Locate every uninfected red blood cell.
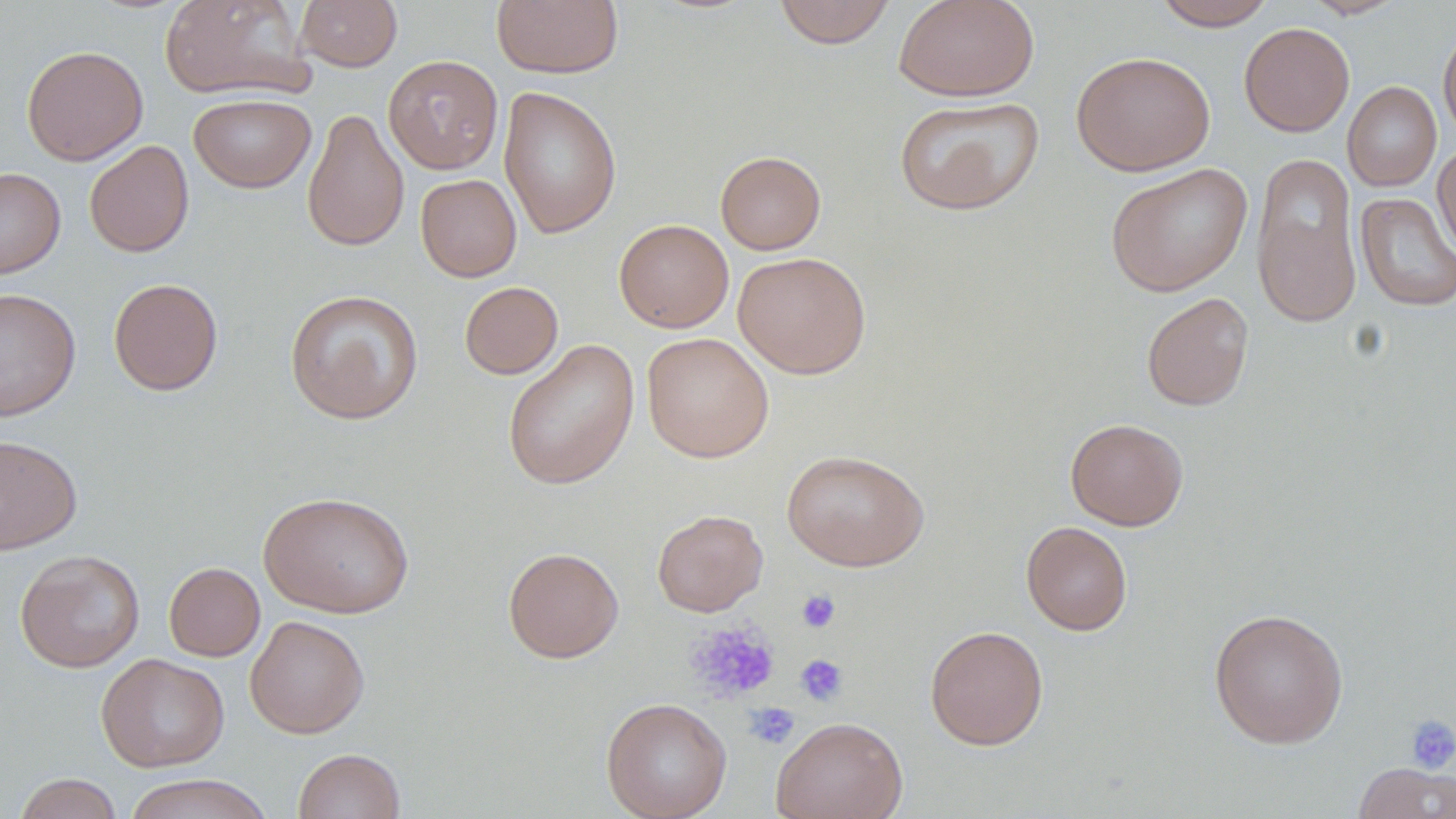
Approximate bounding boxes as (x1, y1, x2, y2) in pixels.
Uninfected red blood cells: (160, 0, 312, 101), (294, 0, 403, 71), (491, 0, 624, 79), (773, 0, 895, 48), (894, 0, 1040, 102), (1152, 0, 1276, 30), (1302, 0, 1408, 19), (1239, 22, 1354, 136), (1438, 23, 1456, 142), (21, 45, 148, 166), (1070, 50, 1216, 176), (383, 55, 503, 174), (1342, 81, 1441, 192), (498, 86, 622, 239), (188, 93, 316, 193), (894, 97, 1043, 215), (302, 107, 409, 252), (84, 140, 194, 258), (1433, 142, 1456, 260), (715, 151, 826, 254), (1251, 151, 1363, 329), (1104, 162, 1253, 297), (0, 167, 65, 279), (415, 174, 522, 282), (1355, 192, 1456, 312), (613, 218, 734, 333), (733, 251, 872, 379), (108, 277, 223, 396), (459, 281, 563, 379), (0, 288, 81, 420), (284, 289, 424, 424), (1141, 292, 1254, 411), (642, 332, 774, 463), (502, 339, 640, 491), (1065, 417, 1189, 530), (0, 434, 83, 555), (781, 449, 930, 571), (259, 490, 414, 618), (652, 509, 768, 616), (1021, 521, 1133, 635), (502, 546, 624, 663), (15, 549, 145, 672), (164, 562, 265, 661), (1208, 607, 1349, 749), (244, 615, 369, 738), (925, 625, 1049, 750), (96, 653, 229, 772), (600, 697, 732, 819), (770, 715, 908, 819), (293, 748, 406, 819), (1353, 762, 1456, 819), (13, 772, 124, 819), (123, 773, 274, 819).

Platelet locations: (796, 589, 841, 633), (685, 621, 781, 704), (794, 653, 849, 706), (744, 703, 800, 749), (1404, 715, 1456, 774). Slide-level diagnosis: no evidence of blood parasites. Thin blood smear. Image is 1456×819 pixels. One field of a larger specimen. 1000x magnification. May-Grünwald-Giemsa-stained preparation. Light microscopy.